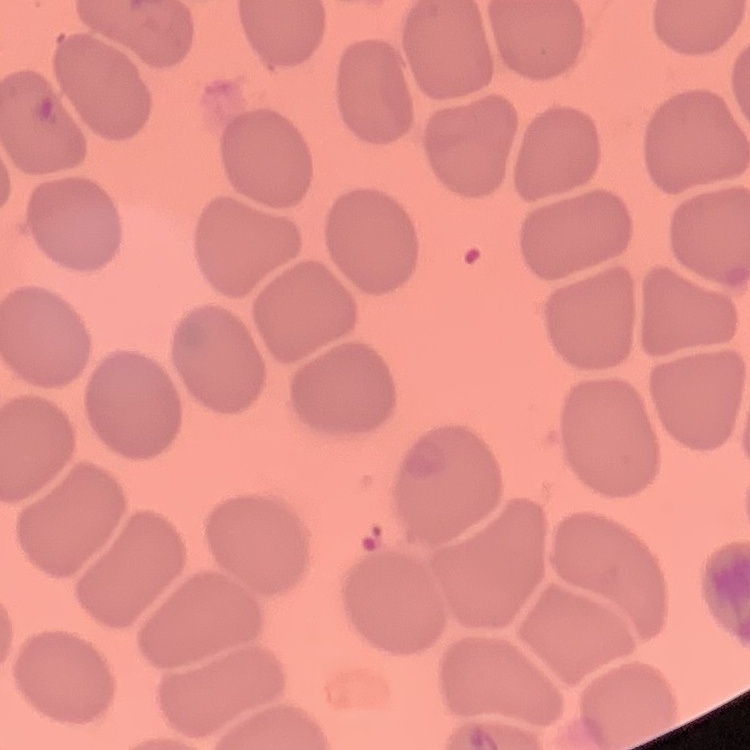
red blood cell morphology = no rouleaux formation
preparation = thin blood film
stain = Field's or Giemsa
image type = square crop of a larger photomicrograph